Outline each Plasmodium vivax-infected red blood cell.
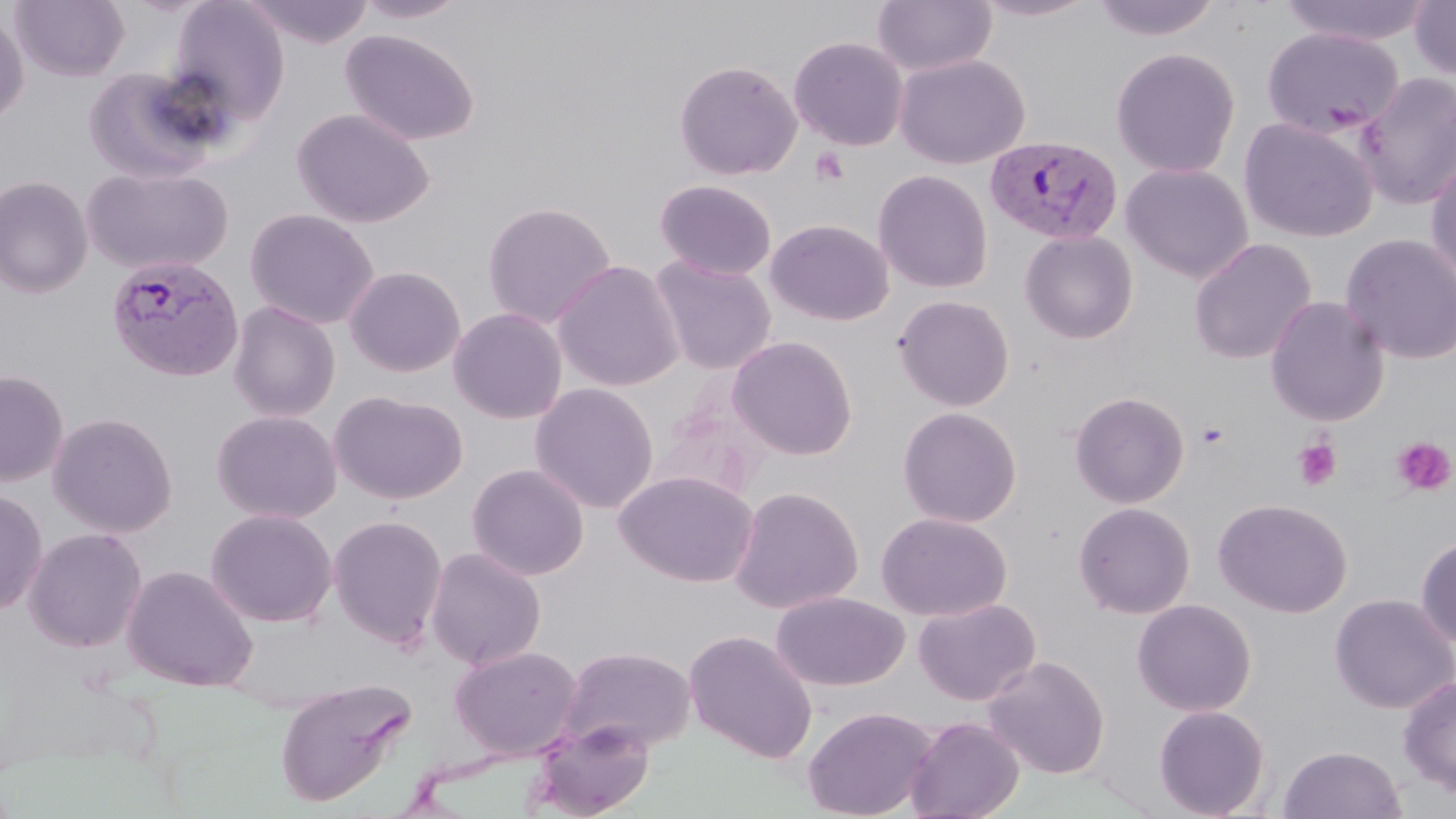

Approximate bounding boxes as (x1, y1, x2, y2) in pixels.
Plasmodium vivax-infected red blood cells: (984, 134, 1123, 245), (106, 252, 244, 381).

slide-level diagnosis = Plasmodium vivax
magnification = 1000x
platelet locations = approximate bounding boxes as (x1, y1, x2, y2) in pixels: (808, 147, 851, 187), (1195, 420, 1230, 450), (1392, 436, 1455, 496), (1292, 437, 1343, 491)
preparation = thin blood film
field of view = one of a larger specimen
uninfected red blood cell locations = approximate bounding boxes as (x1, y1, x2, y2) in pixels: (11, 0, 130, 81), (244, 0, 375, 48), (354, 0, 468, 23), (972, 0, 1102, 22), (1090, 0, 1222, 42), (1278, 0, 1434, 47), (167, 1, 290, 125), (872, 1, 997, 77), (1409, 1, 1456, 81), (0, 9, 29, 124), (1261, 27, 1403, 141), (340, 29, 480, 146), (789, 36, 908, 151), (1110, 47, 1241, 178), (894, 54, 1030, 169), (674, 60, 802, 180), (82, 66, 227, 184), (1354, 71, 1456, 211), (292, 108, 434, 228), (1239, 117, 1378, 243), (1425, 148, 1456, 288), (1120, 163, 1253, 283), (81, 165, 233, 276), (873, 169, 994, 294), (0, 175, 94, 298), (654, 179, 777, 281), (481, 201, 617, 329), (244, 208, 379, 329), (765, 218, 894, 326), (1019, 230, 1138, 344), (1340, 233, 1456, 365), (1188, 238, 1316, 365), (648, 255, 777, 375), (552, 259, 685, 392), (344, 265, 466, 377), (893, 295, 1015, 411), (1264, 296, 1390, 426), (228, 300, 341, 422), (448, 307, 568, 424), (727, 336, 858, 461), (0, 370, 69, 486), (530, 382, 659, 514), (329, 390, 468, 505), (1070, 391, 1189, 508), (897, 406, 1023, 528), (211, 409, 342, 523), (48, 412, 178, 537), (467, 463, 589, 581), (614, 469, 759, 588), (729, 485, 864, 615), (0, 488, 48, 616), (1213, 498, 1352, 618), (1073, 501, 1196, 619), (206, 508, 338, 627), (876, 512, 1012, 622), (328, 515, 448, 649), (23, 527, 148, 652), (1415, 535, 1456, 649), (425, 547, 546, 670), (121, 564, 258, 692), (771, 591, 909, 692), (1329, 594, 1456, 714), (913, 597, 1041, 706), (1132, 598, 1257, 717), (683, 630, 818, 763), (449, 645, 583, 760), (560, 645, 697, 753), (984, 655, 1110, 779), (1397, 675, 1456, 797), (274, 677, 416, 807), (1153, 704, 1270, 818), (802, 705, 936, 819), (905, 716, 1025, 819), (528, 719, 655, 818), (1278, 745, 1407, 819)
stain = May-Grünwald-Giemsa
modality = optical microscopy
image size = 1456×819 pixels